Give the preparation type.
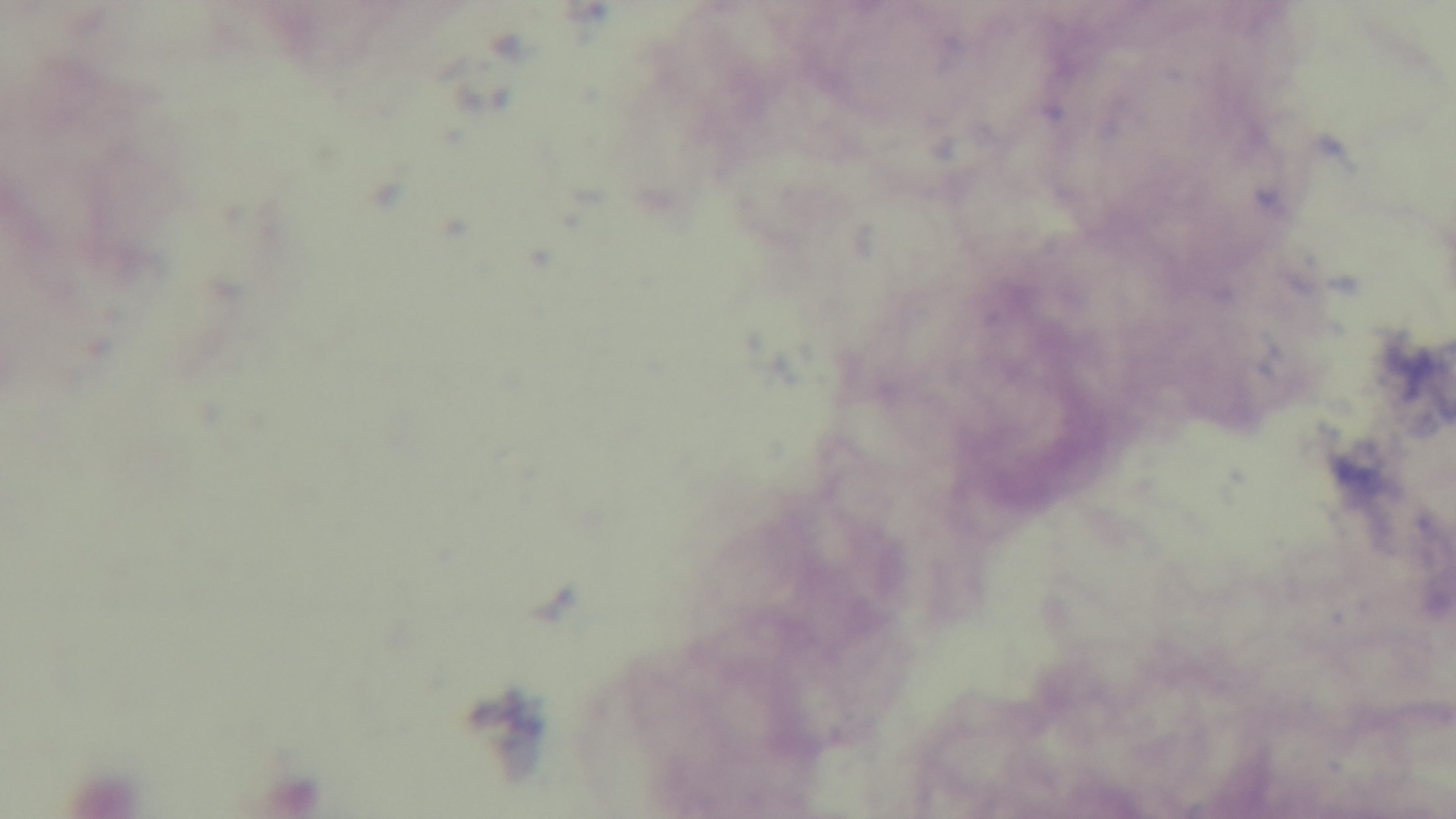
A thick smear.

Single field of view. Photomicrograph. Mounted 4K digital camera. Oil-immersion objective, 100x. Giemsa-stained. Malaria status: uninfected.